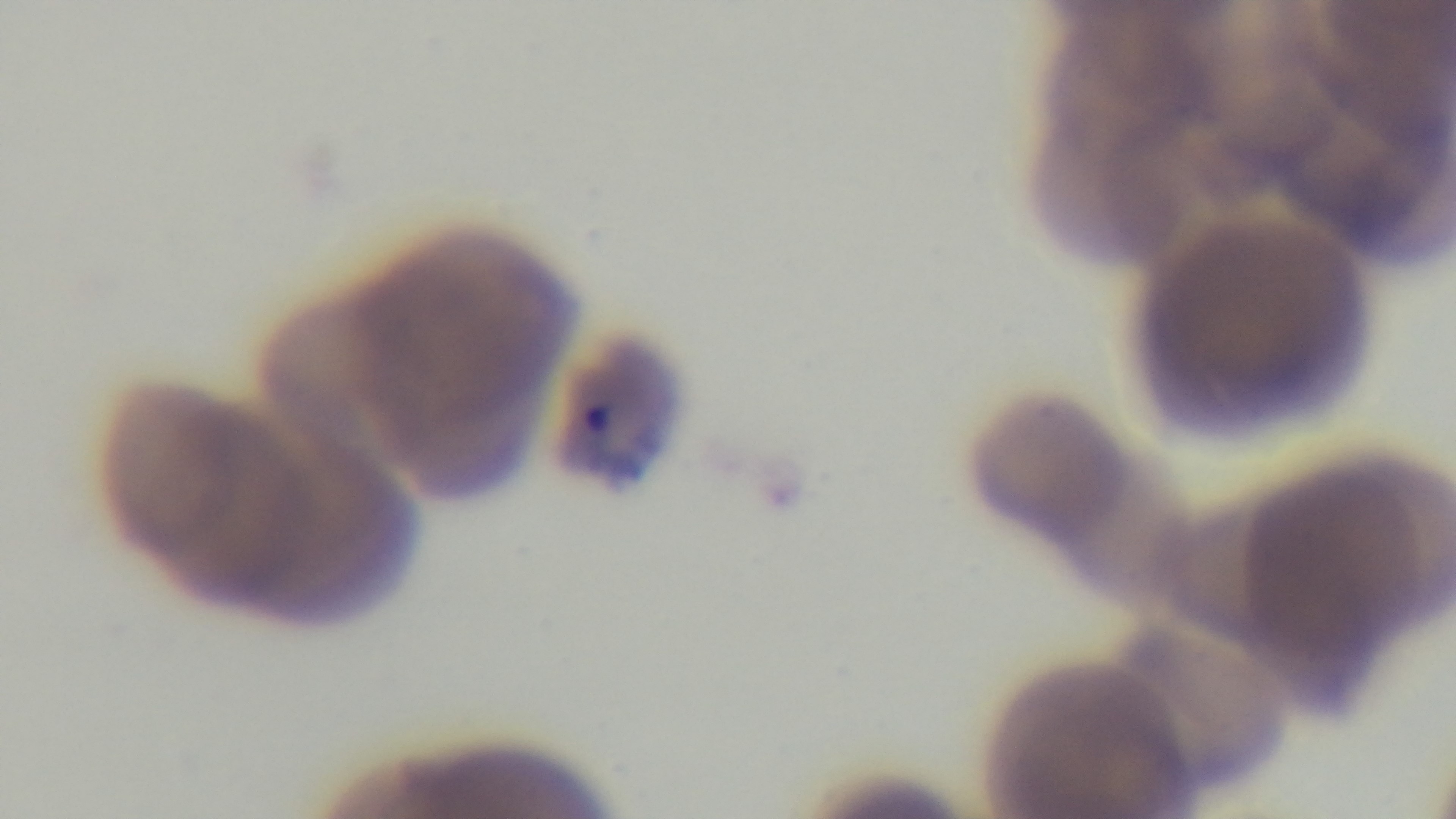

{
  "objective": "100x oil immersion",
  "malaria_status": "infected",
  "stain": "Giemsa",
  "capture": "mounted 4K digital camera",
  "field_of_view": "one from the slide",
  "modality": "light microscopy",
  "preparation": "thin blood film"
}